Classify this cell by malaria status.
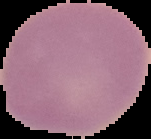

It is uninfected.

The area outside the segmented cell region is set to black. From a thin blood film. Image is 151×139 pixels.